Locate and identify every blood parasite.
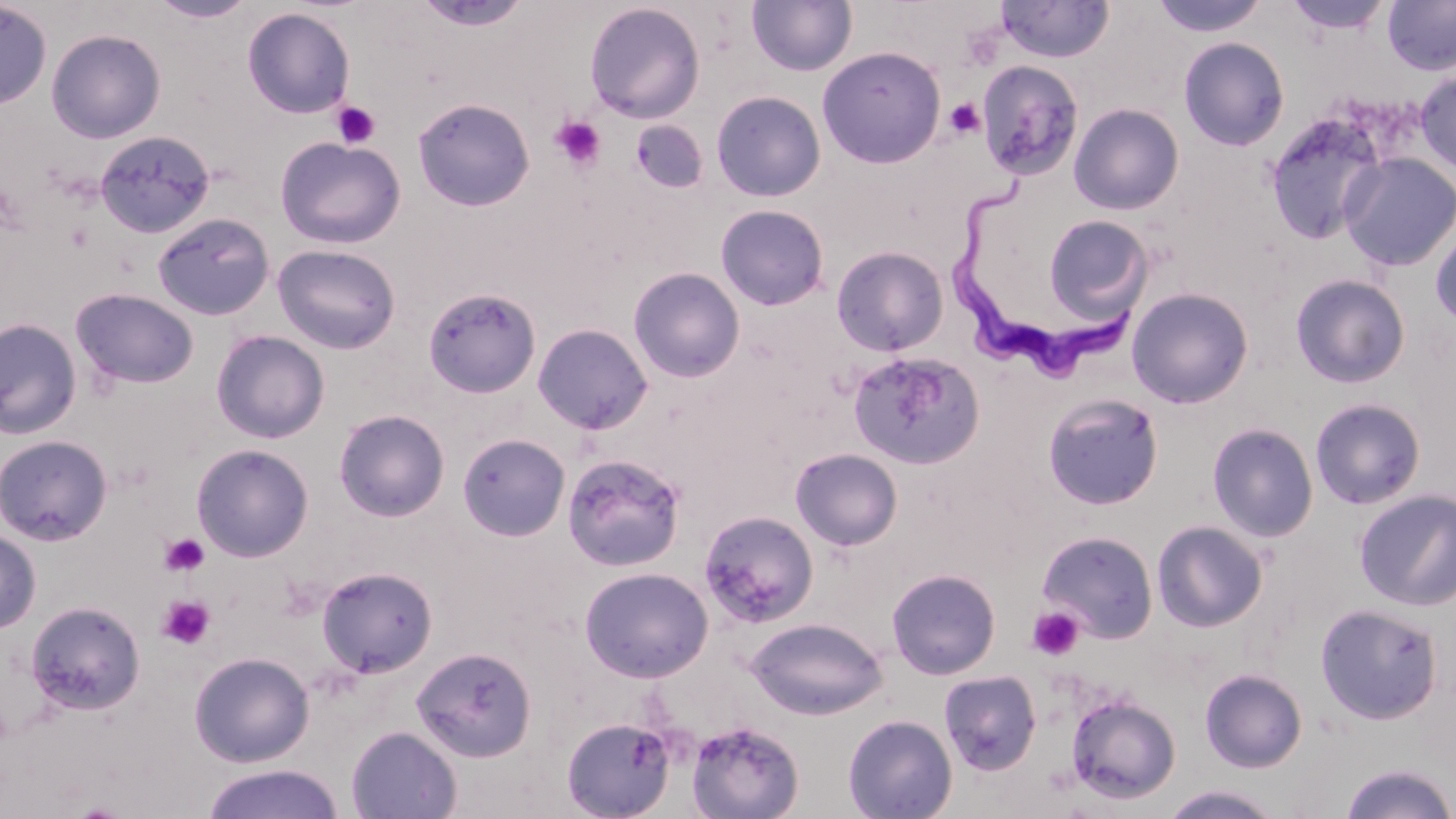
Approximate bounding boxes as (x1, y1, x2, y2) in pixels.
Trypanosoma brucei: (946, 177, 1138, 383).
No Plasmodium falciparum, Plasmodium ovale, Plasmodium malariae, Plasmodium vivax, or Babesia divergens observed.

Uninfected red blood cell locations (subset): (147, 0, 258, 24), (1150, 0, 1269, 38), (1284, 0, 1393, 36), (413, 1, 532, 31), (747, 1, 858, 77), (995, 1, 1115, 63), (1383, 1, 1456, 76), (0, 2, 52, 111), (584, 2, 706, 123), (242, 7, 355, 119), (46, 28, 166, 144), (1178, 36, 1290, 151), (817, 46, 946, 168), (976, 60, 1085, 181), (1415, 70, 1456, 175), (711, 90, 826, 202), (412, 98, 535, 211), (1069, 103, 1185, 215), (1263, 109, 1391, 246), (94, 130, 216, 237), (275, 136, 406, 249), (1338, 152, 1455, 272), (715, 204, 830, 310), (151, 212, 275, 321), (1041, 215, 1154, 324), (1430, 222, 1456, 331), (272, 244, 401, 354), (831, 245, 949, 357), (628, 267, 745, 383), (1290, 273, 1411, 389), (423, 286, 541, 399), (70, 287, 199, 390), (1126, 287, 1254, 409), (0, 318, 82, 440), (532, 323, 653, 435), (211, 330, 330, 444), (848, 350, 985, 470), (1042, 392, 1165, 510), (1309, 397, 1427, 510), (334, 409, 450, 522), (1207, 423, 1319, 542), (457, 432, 570, 541), (0, 434, 114, 545), (191, 443, 314, 562), (790, 447, 903, 551), (562, 453, 686, 573), (1355, 489, 1456, 611), (698, 510, 820, 628), (1152, 520, 1268, 632), (0, 528, 41, 634), (1037, 530, 1159, 643), (316, 566, 437, 678), (580, 566, 713, 682), (886, 568, 1001, 679), (26, 601, 146, 715), (1315, 603, 1443, 725), (746, 617, 886, 719), (411, 646, 537, 763), (189, 651, 315, 767), (1200, 668, 1308, 772), (938, 669, 1042, 776), (1065, 693, 1182, 804), (842, 713, 957, 819), (561, 716, 676, 818), (685, 719, 804, 819), (346, 726, 462, 819), (1339, 762, 1456, 819), (199, 763, 346, 819), (1159, 784, 1287, 819). Platelet locations (subset): (961, 25, 1005, 70), (945, 98, 986, 139), (330, 100, 381, 149), (550, 115, 607, 173), (159, 532, 210, 577), (157, 595, 215, 649), (1026, 607, 1085, 661). Slide-level diagnosis: Trypanosoma brucei. Image is 1456×819 pixels. May-Grünwald-Giemsa stain. One field of a larger specimen. 1000x magnification. Thin blood film. Light microscopy.